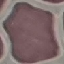
Result: no malaria parasites seen. Photographed with a smartphone camera at the microscope eyepiece. Automatically extracted cell patch, resized to 64 × 64 pixels. Giemsa-stained preparation. Thin smear of blood.